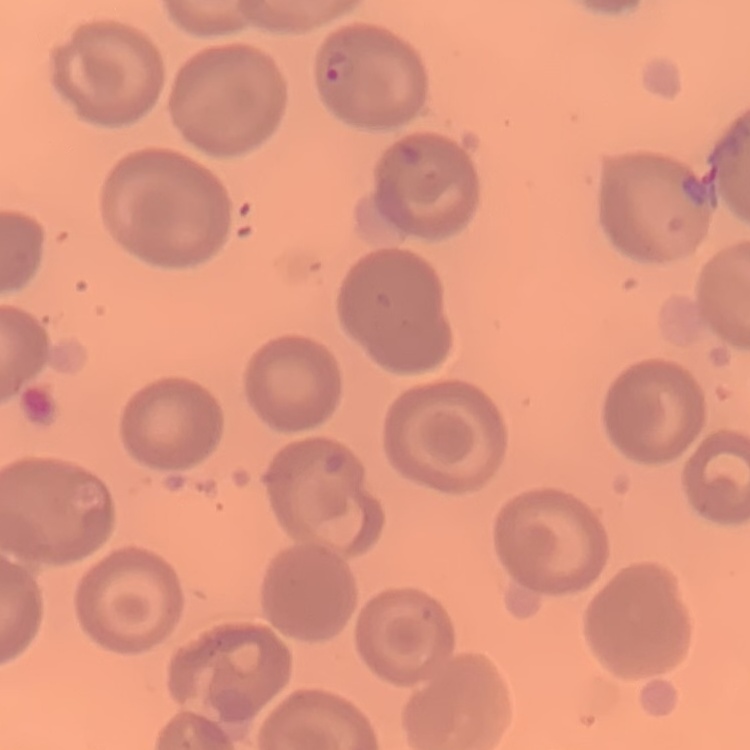

erythrocyte morphology = no rouleaux formation
image type = square crop of a larger photomicrograph
preparation = thin blood film
stain = Field's or Giemsa